Locate every Plasmodium falciparum parasite and identify its life-cycle stage.
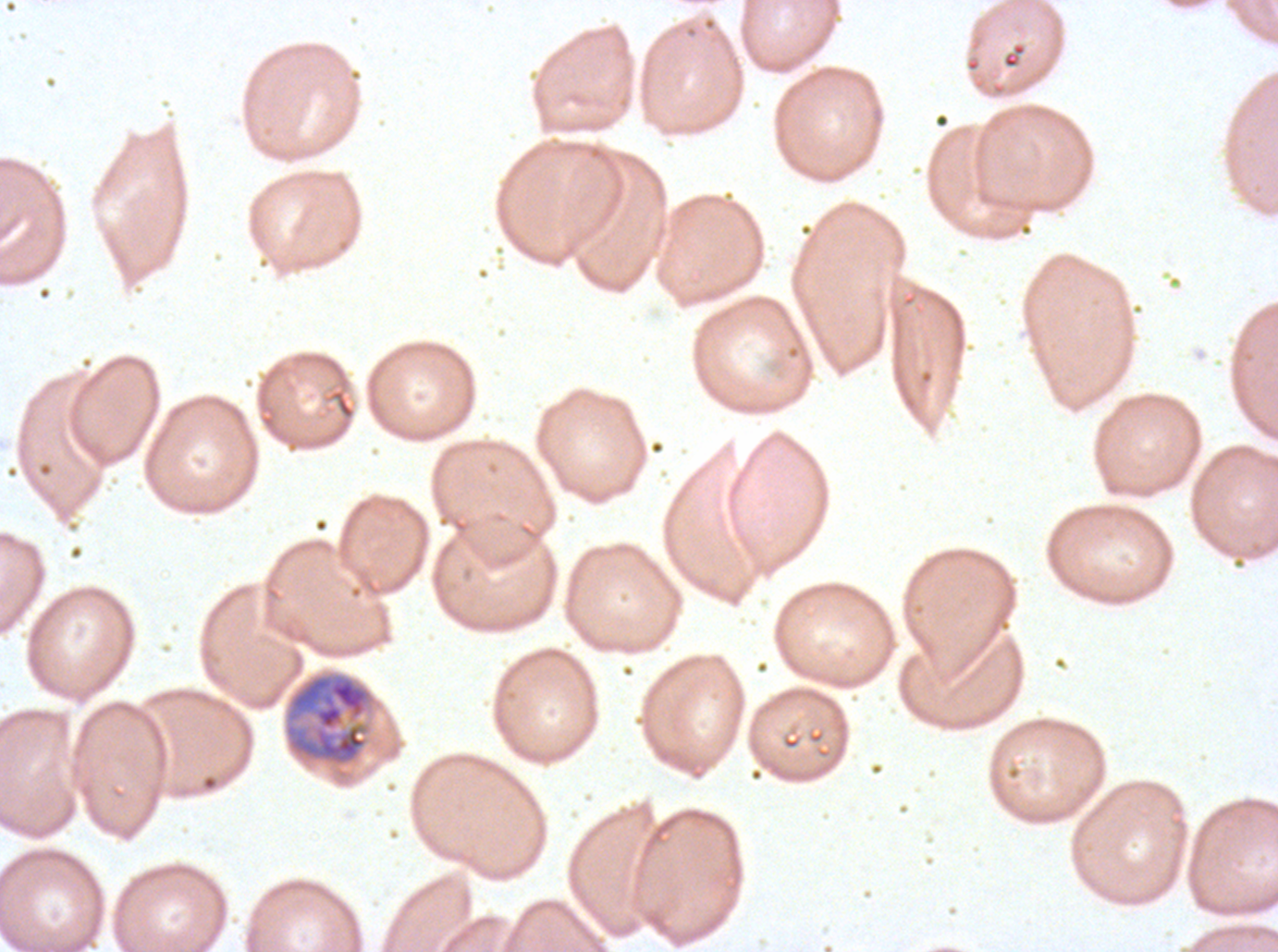

Approximate bounding boxes as (x1, y1, x2, y2) in pixels.
Late trophozoites: (283, 671, 376, 767).
No rings, late-ring/early-trophozoite forms, mid trophozoites, early schizonts, late schizonts, segmenters, or gametocytes observed.

Summary:
  - Preparation: thin blood film
  - Image size: 1278×952 pixels
  - Field of view: sub-image separated from a larger composite
  - Specimen: Plasmodium falciparum cultured ex vivo for 24 to 48 hours, from a patient in The Gambia
  - Stain: Giemsa